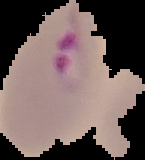

image_type: segmented cell region on a black background
preparation: thin blood film
result: Plasmodium parasites identified
image_size: 145×160 pixels